Identify the parasite.
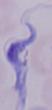
This is a trypanosome.

Photomicrograph. Captured at 1000x magnification.